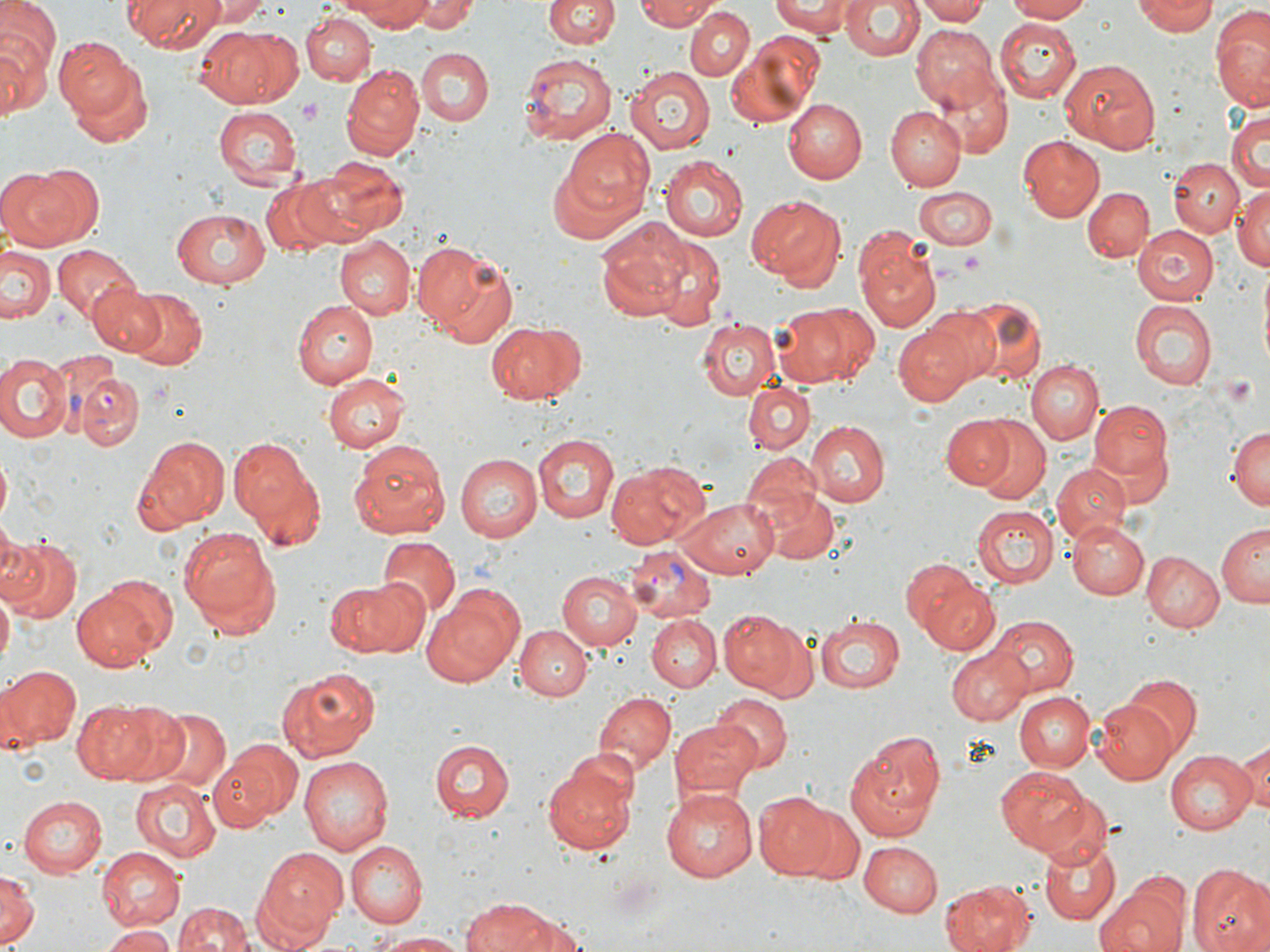

slide-level diagnosis = Plasmodium vivax
preparation = thin blood film
uninfected red blood cell locations = approximate bounding boxes as (x1,y1)-(x2,y2) corner pairs in pixels: (124,0)-(222,51), (204,0)-(270,26), (335,0)-(444,31), (411,0)-(473,32), (544,0)-(619,49), (636,0)-(721,31), (771,0)-(857,36), (841,0)-(924,63), (915,0)-(989,25), (1005,0)-(1090,22), (1132,0)-(1215,36), (1,1)-(59,78), (129,2)-(273,79), (684,2)-(795,115), (685,6)-(755,80), (1210,8)-(1270,109), (301,13)-(375,85), (994,18)-(1081,103), (189,24)-(298,107), (912,25)-(1002,111), (0,30)-(50,121), (726,33)-(823,126), (56,37)-(137,118), (417,47)-(495,127), (65,58)-(152,147), (1059,59)-(1162,153), (342,64)-(423,157), (932,66)-(1013,155), (626,67)-(715,153), (785,99)-(868,182), (213,107)-(302,188), (887,109)-(964,190), (1226,109)-(1269,195), (564,128)-(656,215), (1019,136)-(1103,222), (659,156)-(749,242), (311,157)-(410,237), (1171,158)-(1244,238), (0,163)-(99,250), (549,164)-(638,246), (261,177)-(349,253), (1082,186)-(1154,263), (1231,186)-(1270,271), (912,187)-(999,248), (746,195)-(843,288), (169,209)-(270,288), (598,223)-(688,320), (1134,224)-(1222,305), (853,227)-(941,330), (648,233)-(728,329), (333,236)-(415,320), (416,243)-(520,346), (53,244)-(138,322), (1,247)-(57,327), (89,282)-(165,356), (123,287)-(208,372), (951,295)-(1044,384), (295,299)-(379,387), (1128,299)-(1218,391), (771,303)-(874,389), (697,319)-(780,400), (892,319)-(989,405), (484,321)-(585,405), (0,353)-(73,443), (1029,361)-(1103,446), (324,372)-(411,453), (745,381)-(815,454), (1090,397)-(1173,491), (942,411)-(1024,494), (971,418)-(1051,505), (805,421)-(890,507), (1227,425)-(1269,512), (132,433)-(230,533), (230,435)-(318,538), (532,435)-(620,522), (347,440)-(451,537), (456,453)-(542,542), (740,453)-(828,540), (0,454)-(11,526), (606,462)-(710,549), (1050,464)-(1131,542), (765,490)-(839,563), (673,496)-(776,579), (970,504)-(1056,589), (1068,520)-(1148,600), (177,524)-(280,632), (1216,524)-(1269,607), (0,535)-(83,623), (376,537)-(461,621), (1140,551)-(1224,633), (556,570)-(643,650), (914,570)-(1001,657), (102,572)-(177,654), (322,578)-(425,659), (0,586)-(13,672), (425,586)-(526,687), (72,587)-(167,671), (717,609)-(808,697), (814,615)-(905,695), (987,615)-(1077,696), (646,616)-(720,691), (516,625)-(589,701), (948,648)-(1029,725), (0,664)-(80,749), (277,665)-(383,761), (1122,674)-(1202,754), (593,691)-(675,774), (1012,691)-(1094,772), (712,695)-(792,774), (1092,697)-(1179,784), (72,700)-(169,784), (144,707)-(233,791), (671,718)-(763,798), (845,730)-(946,837), (431,738)-(514,822), (214,739)-(303,828), (1231,741)-(1268,821), (543,749)-(641,855), (1166,750)-(1257,833), (299,756)-(395,856), (994,766)-(1095,857), (132,776)-(219,864), (1024,782)-(1117,871), (660,786)-(757,883), (755,792)-(835,879), (19,795)-(110,878), (786,804)-(863,883), (1038,836)-(1118,925), (344,840)-(427,926), (862,840)-(942,916), (96,847)-(186,930), (254,847)-(348,944), (1188,865)-(1270,952), (0,870)-(39,950), (941,879)-(1037,952), (1093,884)-(1189,952), (464,896)-(562,952), (173,900)-(254,952), (499,910)-(585,951), (101,925)-(175,952), (373,931)-(472,950)
magnification = 1000x
Plasmodium vivax-infected red blood cell locations = approximate bounding boxes as (x1,y1)-(x2,y2) corner pairs in pixels: (518,52)-(619,144), (71,370)-(146,451), (624,544)-(717,623)
field of view = single
modality = light microscopy
platelet locations = approximate bounding boxes as (x1,y1)-(x2,y2) corner pairs in pixels: (297,101)-(323,125), (962,251)-(982,269)
image size = 1270×952 pixels
stain = May-Grünwald-Giemsa